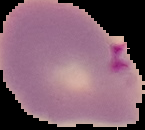
Summary:
  - Image size: 145×130 pixels
  - Malaria status: parasitized
  - Preparation: thin blood smear
  - Image type: segmented cell region with the area outside set to black